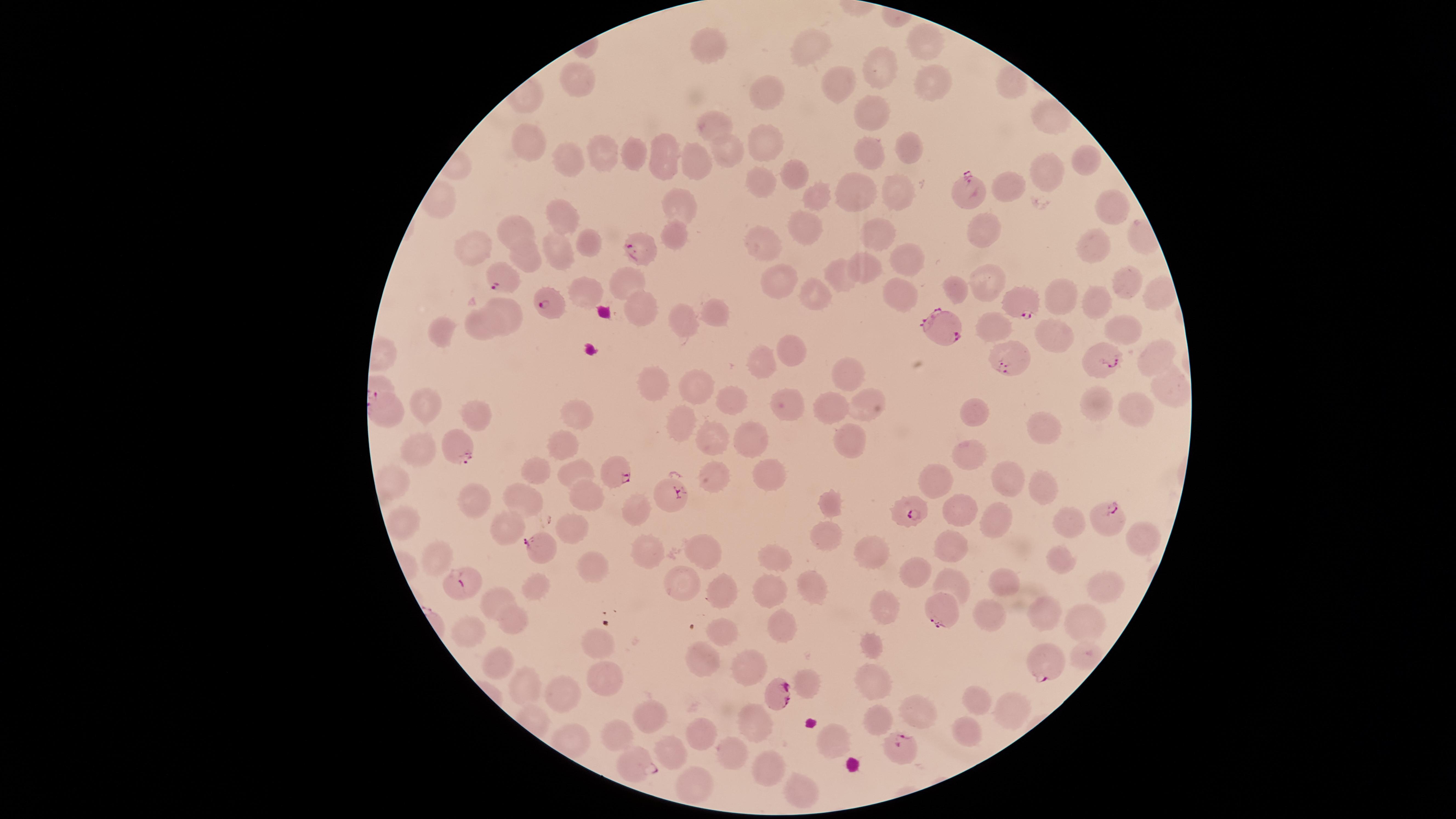 Approximate marker points as {x, y} in pixels. Uninfected red blood cells: {928, 39}, {713, 52}, {813, 52}, {881, 63}, {581, 74}, {835, 84}, {925, 84}, {1009, 84}, {768, 88}, {861, 115}, {1049, 118}, {713, 119}, {763, 140}, {522, 144}, {906, 148}, {727, 149}, {601, 152}, {636, 155}, {571, 159}, {661, 159}, {873, 159}, {701, 161}, {1082, 162}, {795, 174}, {1046, 174}, {761, 179}, {1005, 187}, {812, 189}, {899, 194}, {859, 195}, {685, 200}, {1111, 210}, {557, 213}, {807, 225}, {518, 228}, {881, 232}, {676, 234}, {974, 234}, {1091, 238}, {768, 242}, {586, 245}, {477, 249}, {556, 249}, {527, 258}, {914, 261}, {865, 264}, {844, 268}, {993, 278}, {1121, 279}, {624, 281}, {778, 282}, {823, 284}, {586, 285}, {959, 287}, {900, 290}, {1063, 293}, {1097, 299}, {640, 304}, {509, 310}, {715, 310}, {685, 321}, {997, 325}, {488, 326}, {1116, 328}, {442, 335}, {1059, 335}, {1150, 351}, {798, 353}, {754, 362}, {846, 372}, {661, 374}, {698, 386}, {1173, 390}, {732, 397}, {786, 399}, {1099, 400}, {863, 405}, {1137, 406}, {834, 407}, {973, 408}, {428, 409}, {577, 412}, {476, 415}, {676, 415}, {1040, 423}, {848, 430}, {748, 435}, {714, 437}, {560, 445}, {425, 453}, {963, 455}, {540, 470}, {573, 472}, {761, 472}, {715, 473}, {1006, 476}, {935, 478}, {1037, 485}, {587, 491}, {527, 494}, {475, 500}, {833, 501}, {637, 510}, {957, 511}, {991, 518}, {405, 521}, {503, 523}, {1064, 525}, {564, 527}, {820, 533}, {952, 538}, {1142, 538}, {701, 544}, {646, 545}, {867, 545}, {776, 553}, {437, 560}, {585, 563}, {1064, 564}, {917, 571}, {681, 579}, {809, 581}, {949, 581}, {1109, 586}, {720, 587}, {535, 588}, {770, 589}, {1004, 591}, {497, 594}, {881, 602}, {1041, 609}, {516, 614}, {988, 617}, {779, 620}, {1085, 621}, {724, 624}, {476, 631}, {594, 641}, {874, 647}, {709, 648}, {497, 653}, {604, 666}, {754, 666}, {877, 682}, {811, 683}, {522, 684}, {561, 691}, {977, 707}, {1007, 709}, {929, 713}, {649, 714}, {754, 717}, {877, 718}, {702, 730}, {571, 731}, {622, 734}, {835, 735}, {967, 735}, {674, 749}, {732, 752}, {763, 765}, {691, 781}, {791, 786}. Parasitized red blood cells: {967, 191}, {642, 247}, {498, 276}, {1020, 300}, {550, 306}, {941, 323}, {1109, 357}, {1014, 358}, {455, 446}, {617, 468}, {669, 495}, {910, 504}, {1104, 516}, {538, 548}, {462, 584}, {941, 606}, {1047, 661}, {776, 692}, {902, 742}, {635, 762}. One field of view of the specimen. Species: Plasmodium falciparum. Thin blood smear. Giemsa stain. Image is 1456×819 pixels. Photographed with a smartphone camera through the microscope eyepiece. Presence: malaria parasites detected. The visible region is circular.